Name the parasite shown.
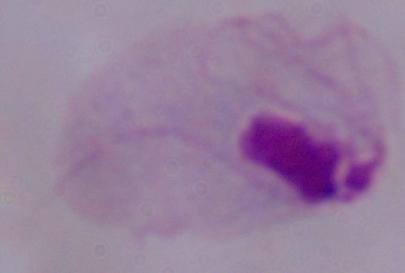

A trichomonad.

Summary:
  - Modality: photomicrograph
  - Magnification: 1000x